Name the blood parasite species.
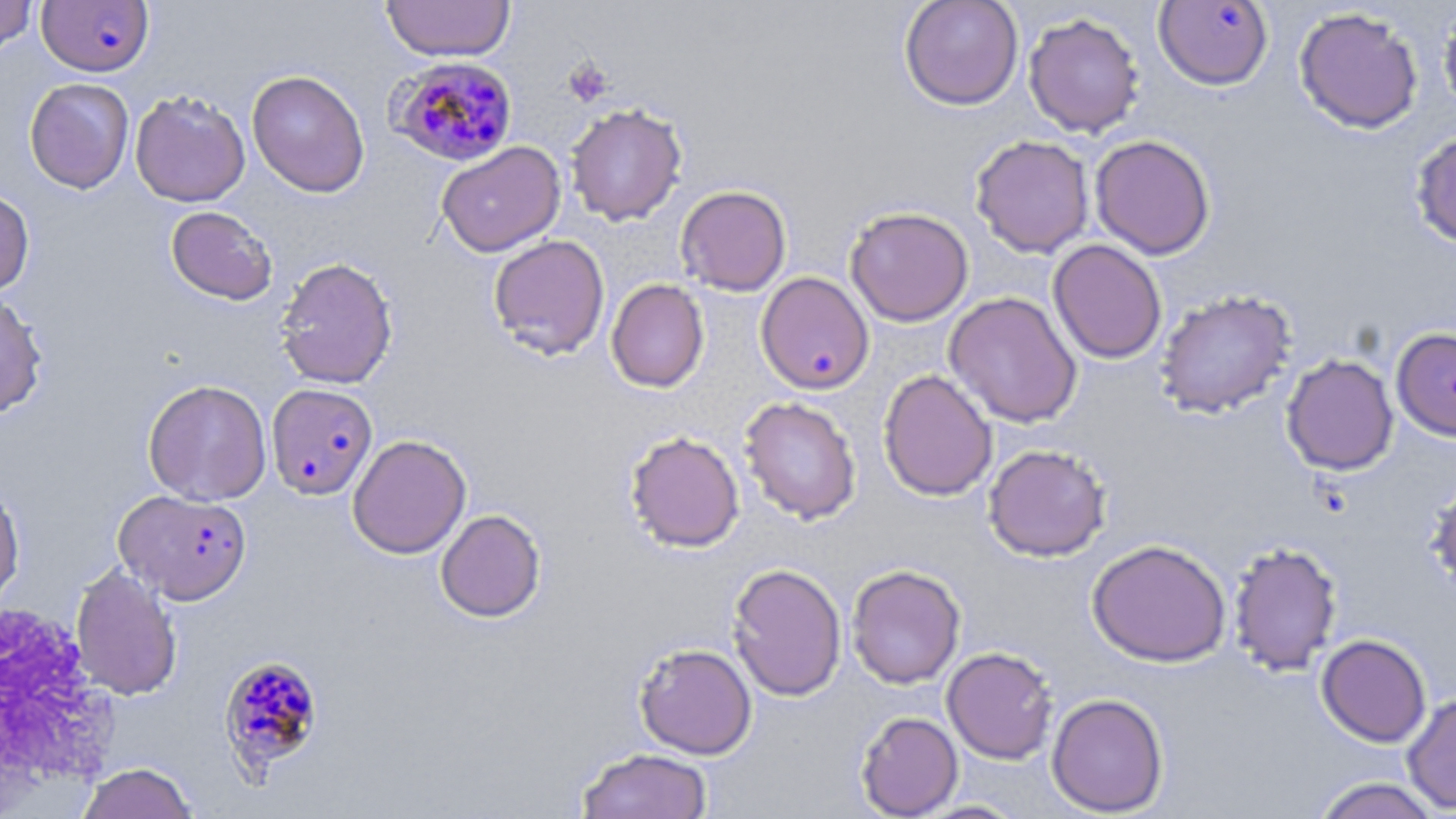
Plasmodium falciparum.

modality = light microscopy
image size = 1456×819 pixels
magnification = 1000x
Plasmodium falciparum-infected red blood cell locations (subset) = approximate bounding boxes as (x1,y1)-(x2,y2) corner pairs in pixels: (37,1)-(153,76), (1154,1)-(1273,91), (387,56)-(519,166), (755,271)-(875,394), (267,383)-(378,500), (115,489)-(253,604)
white blood cell locations = approximate bounding boxes as (x1,y1)-(x2,y2) corner pairs in pixels: (0,597)-(121,807)
uninfected red blood cell locations = approximate bounding boxes as (x1,y1)-(x2,y2) corner pairs in pixels: (381,0)-(516,62), (899,0)-(1023,110), (0,1)-(38,54), (1437,3)-(1456,119), (1294,6)-(1424,134), (1023,12)-(1145,138), (246,70)-(370,197), (23,77)-(134,194), (130,89)-(250,207), (565,103)-(687,226), (1410,128)-(1456,250), (1089,134)-(1216,260), (970,135)-(1094,258), (437,141)-(565,257), (675,185)-(792,296), (0,188)-(35,297), (166,206)-(277,304), (845,206)-(974,326), (488,234)-(610,360), (1048,239)-(1167,364), (275,256)-(399,389), (606,279)-(709,393), (1154,289)-(1297,419), (944,291)-(1083,429), (0,292)-(48,419), (1390,326)-(1456,441), (1281,354)-(1399,476), (878,369)-(998,501), (143,379)-(272,506), (739,396)-(862,525), (624,430)-(745,553), (348,434)-(472,559), (983,444)-(1112,561), (1425,471)-(1456,597), (0,480)-(24,609), (435,509)-(546,622), (1087,539)-(1231,667), (1227,540)-(1343,676), (727,562)-(847,701), (70,563)-(183,701), (846,564)-(966,689), (1316,634)-(1431,747), (633,642)-(757,759), (941,646)-(1058,764), (1047,693)-(1168,816), (1401,693)-(1456,814), (855,711)-(963,818), (576,748)-(713,819), (75,762)-(199,819), (1310,776)-(1445,819), (912,799)-(1028,818)
platelet locations (subset) = approximate bounding boxes as (x1,y1)-(x2,y2) corner pairs in pixels: (563,59)-(612,107)
preparation = thin blood smear
stain = May-Grünwald-Giemsa
field of view = single